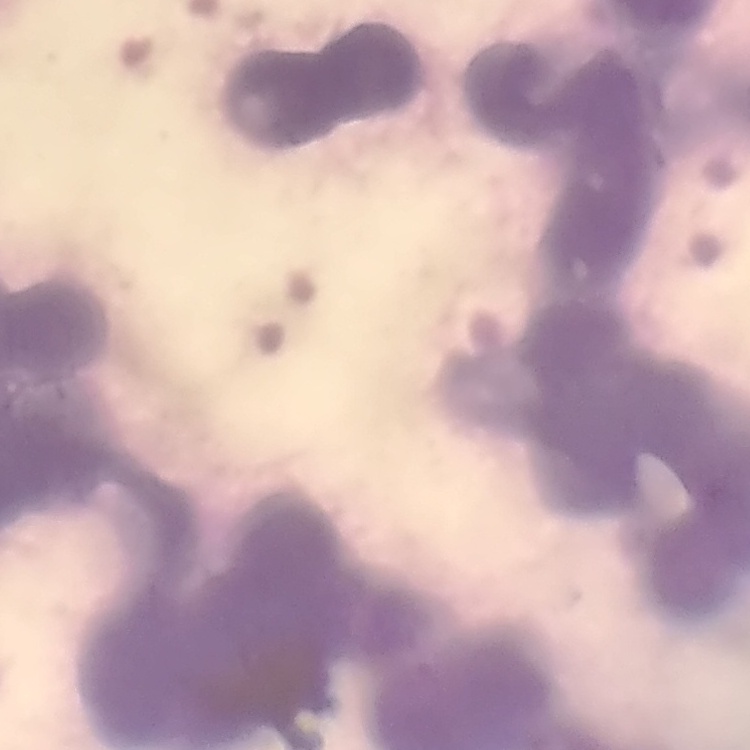

erythrocyte morphology = rouleaux formation
preparation = thin peripheral smear
stain = Field's or Giemsa
image type = one tile cut from a larger photomicrograph